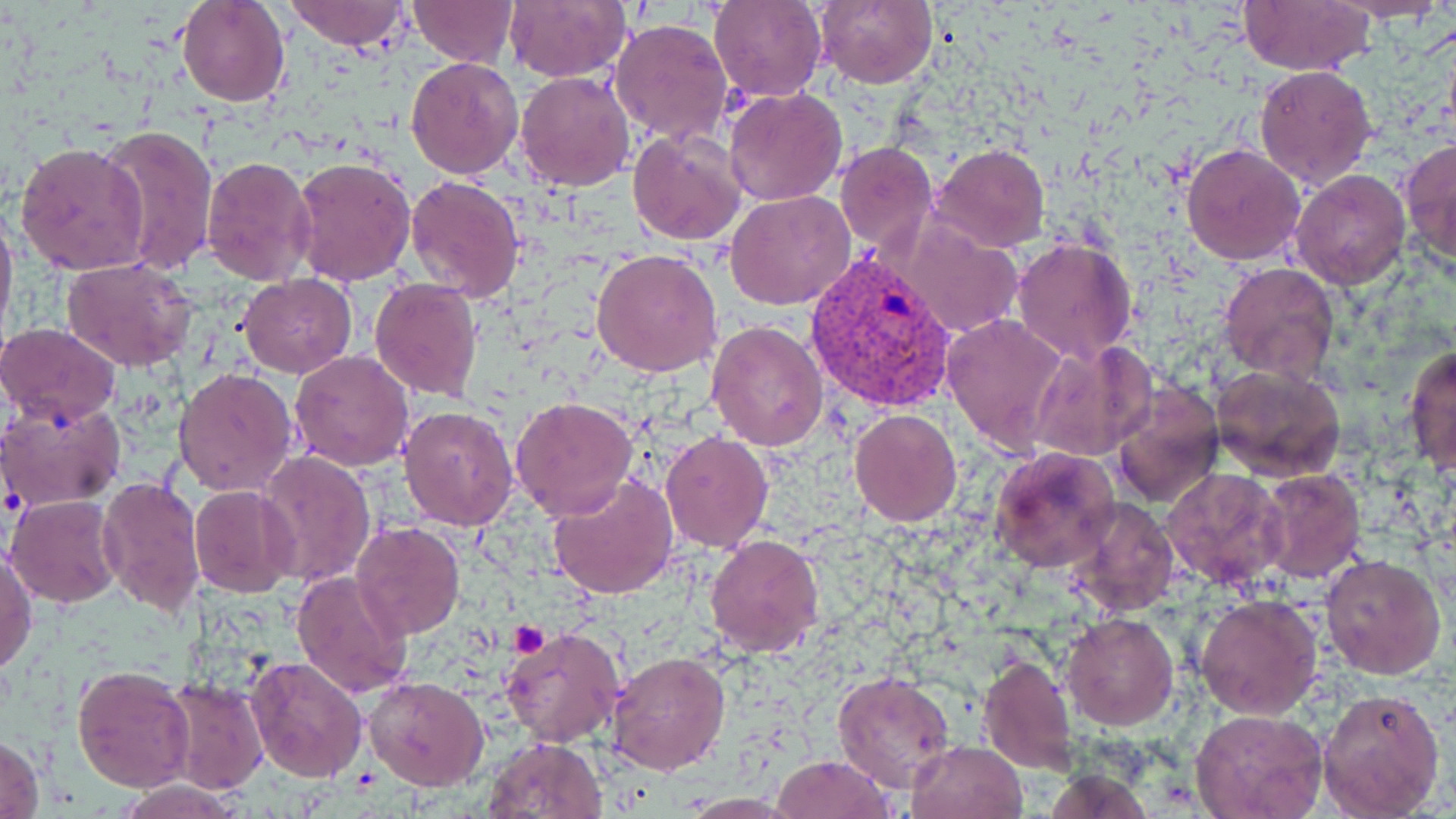
slide-level diagnosis = Plasmodium vivax
magnification = 1000x
Plasmodium vivax-infected red blood cell locations = approximate bounding boxes as (x1, y1, x2, y2) in pixels: (804, 248, 960, 414)
stain = May-Grünwald-Giemsa
uninfected red blood cell locations = approximate bounding boxes as (x1, y1, x2, y2) in pixels: (176, 0, 290, 107), (280, 0, 412, 51), (505, 0, 630, 82), (710, 0, 826, 102), (815, 0, 937, 90), (1332, 0, 1449, 25), (406, 1, 520, 67), (1236, 1, 1376, 74), (610, 18, 734, 147), (405, 55, 525, 178), (1254, 64, 1378, 190), (514, 69, 635, 192), (724, 87, 848, 206), (97, 125, 217, 277), (627, 131, 746, 245), (1401, 137, 1456, 268), (16, 141, 150, 276), (834, 141, 937, 254), (932, 142, 1050, 253), (1181, 142, 1306, 266), (202, 156, 318, 287), (291, 156, 416, 286), (1291, 169, 1411, 290), (406, 175, 525, 302), (724, 191, 856, 311), (0, 202, 18, 343), (888, 212, 1023, 339), (1012, 237, 1137, 364), (592, 247, 723, 378), (62, 257, 197, 370), (1218, 263, 1340, 383), (238, 274, 358, 377), (369, 277, 482, 404), (943, 312, 1070, 452), (706, 319, 831, 451), (0, 322, 122, 426), (1029, 340, 1157, 462), (1404, 343, 1456, 479), (289, 350, 415, 472), (1211, 363, 1346, 482), (173, 367, 299, 498), (1109, 380, 1224, 510), (509, 396, 639, 520), (0, 398, 127, 510), (398, 406, 519, 530), (849, 409, 962, 527), (660, 431, 772, 551), (989, 444, 1120, 574), (256, 450, 377, 589), (1161, 467, 1289, 592), (1257, 468, 1366, 584), (546, 473, 680, 600), (98, 477, 206, 618), (189, 485, 301, 598), (6, 495, 124, 607), (1066, 497, 1179, 617), (352, 521, 465, 639), (705, 533, 824, 658), (1, 545, 37, 676), (1321, 553, 1448, 679), (290, 570, 413, 698), (1195, 593, 1324, 721), (1062, 613, 1178, 729), (500, 625, 625, 749), (606, 649, 730, 776), (977, 652, 1072, 777), (246, 656, 369, 783), (71, 663, 196, 792), (833, 670, 958, 794), (365, 675, 489, 790), (159, 676, 269, 793), (1318, 687, 1446, 817), (1191, 709, 1329, 819), (0, 734, 47, 818), (481, 737, 606, 819), (906, 739, 1028, 819), (770, 755, 896, 818), (113, 779, 250, 818)
preparation = thin blood film
platelet locations = approximate bounding boxes as (x1, y1, x2, y2) in pixels: (507, 623, 549, 655)
modality = optical microscopy
field of view = one of a larger specimen
image size = 1456×819 pixels